Report the malaria status of this cell.
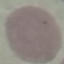

Uninfected.

Summary:
  - Image type: automatically extracted cell patch, resized to 64 × 64 pixels
  - Stain: Giemsa
  - Capture: smartphone camera at the microscope eyepiece
  - Preparation: thin smear